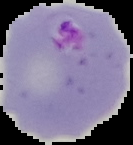
Summary:
  - Malaria status: parasitized
  - Image type: segmented cell region on a black background
  - Preparation: thin blood film
  - Image size: 133×145 pixels